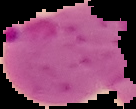
Summary:
  - Malaria status: parasitized
  - Preparation: thin blood film
  - Image type: cell region segmented out of the field of view; surrounding area masked to black
  - Image size: 136×109 pixels